Name the parasite shown.
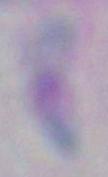
Toxoplasma gondii.

Summary:
  - Modality: micrograph
  - Magnification: 1000x